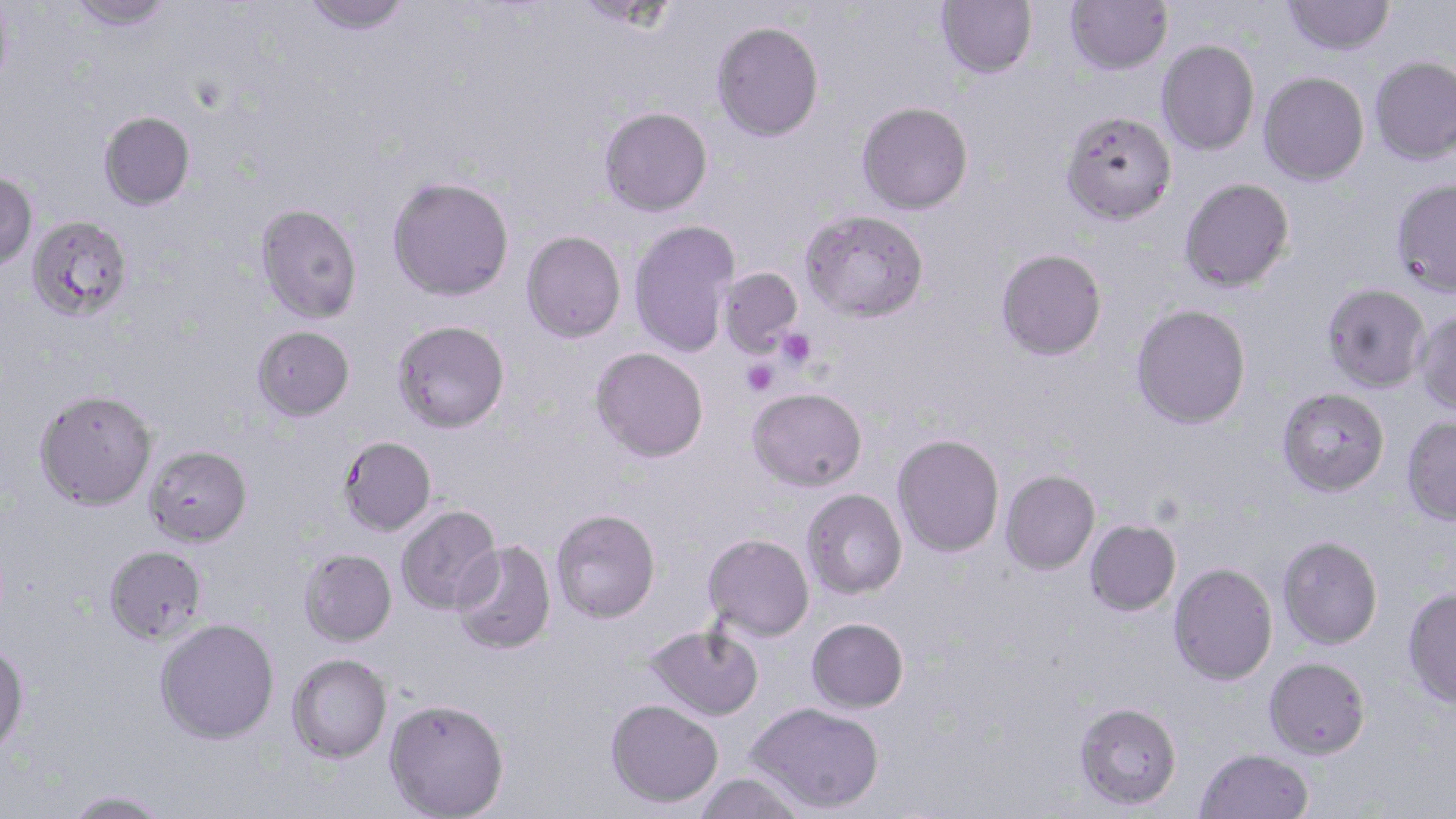
slide-level diagnosis = Plasmodium falciparum
uninfected red blood cell locations = approximate bounding boxes as (x1, y1, x2, y2) in pixels: (0, 0, 13, 94), (67, 0, 174, 30), (302, 0, 412, 36), (573, 0, 680, 32), (936, 0, 1037, 79), (1065, 0, 1173, 75), (1283, 0, 1395, 55), (711, 21, 824, 142), (1156, 39, 1259, 156), (1370, 56, 1456, 165), (1258, 71, 1369, 185), (857, 102, 973, 215), (599, 106, 712, 216), (1060, 110, 1177, 225), (98, 111, 195, 211), (0, 171, 38, 270), (387, 176, 514, 301), (1178, 177, 1295, 293), (1391, 178, 1456, 297), (255, 203, 362, 323), (800, 209, 930, 322), (26, 215, 133, 322), (629, 220, 738, 357), (521, 230, 626, 343), (995, 248, 1107, 360), (718, 267, 804, 358), (1322, 283, 1431, 392), (1131, 304, 1251, 429), (1414, 310, 1456, 416), (391, 320, 510, 433), (252, 325, 355, 421), (591, 347, 709, 462), (747, 386, 867, 491), (1277, 387, 1390, 496), (34, 389, 158, 511), (1402, 416, 1456, 525), (892, 434, 1005, 557), (339, 435, 437, 536), (144, 444, 252, 546), (1000, 470, 1100, 575), (801, 488, 907, 599), (395, 505, 503, 616), (550, 509, 661, 623), (1084, 519, 1181, 616), (703, 533, 814, 640), (1278, 535, 1383, 649), (450, 540, 557, 656), (102, 545, 208, 645), (299, 548, 397, 646), (1169, 563, 1277, 685), (1402, 587, 1456, 708), (154, 617, 280, 743), (806, 617, 908, 713), (645, 624, 763, 721), (0, 642, 29, 755), (287, 653, 392, 763), (1264, 657, 1370, 759), (384, 698, 510, 818), (605, 698, 723, 808), (746, 701, 885, 813), (1074, 702, 1182, 810), (1195, 748, 1313, 819), (693, 771, 808, 818), (61, 790, 170, 819)
preparation = thin blood smear
stain = May-Grünwald-Giemsa
modality = optical microscopy
image size = 1456×819 pixels
field of view = one of a larger specimen
magnification = 1000x
platelet locations = approximate bounding boxes as (x1, y1, x2, y2) in pixels: (776, 328, 816, 369), (742, 359, 778, 396)